Identify the parasite.
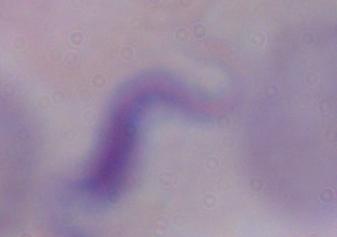

This is a trypanosome.

Summary:
  - Modality: photomicrograph
  - Magnification: 1000x